Locate the cells, classifying each as a parasitized RBC, an uninfected RBC, or a WBC.
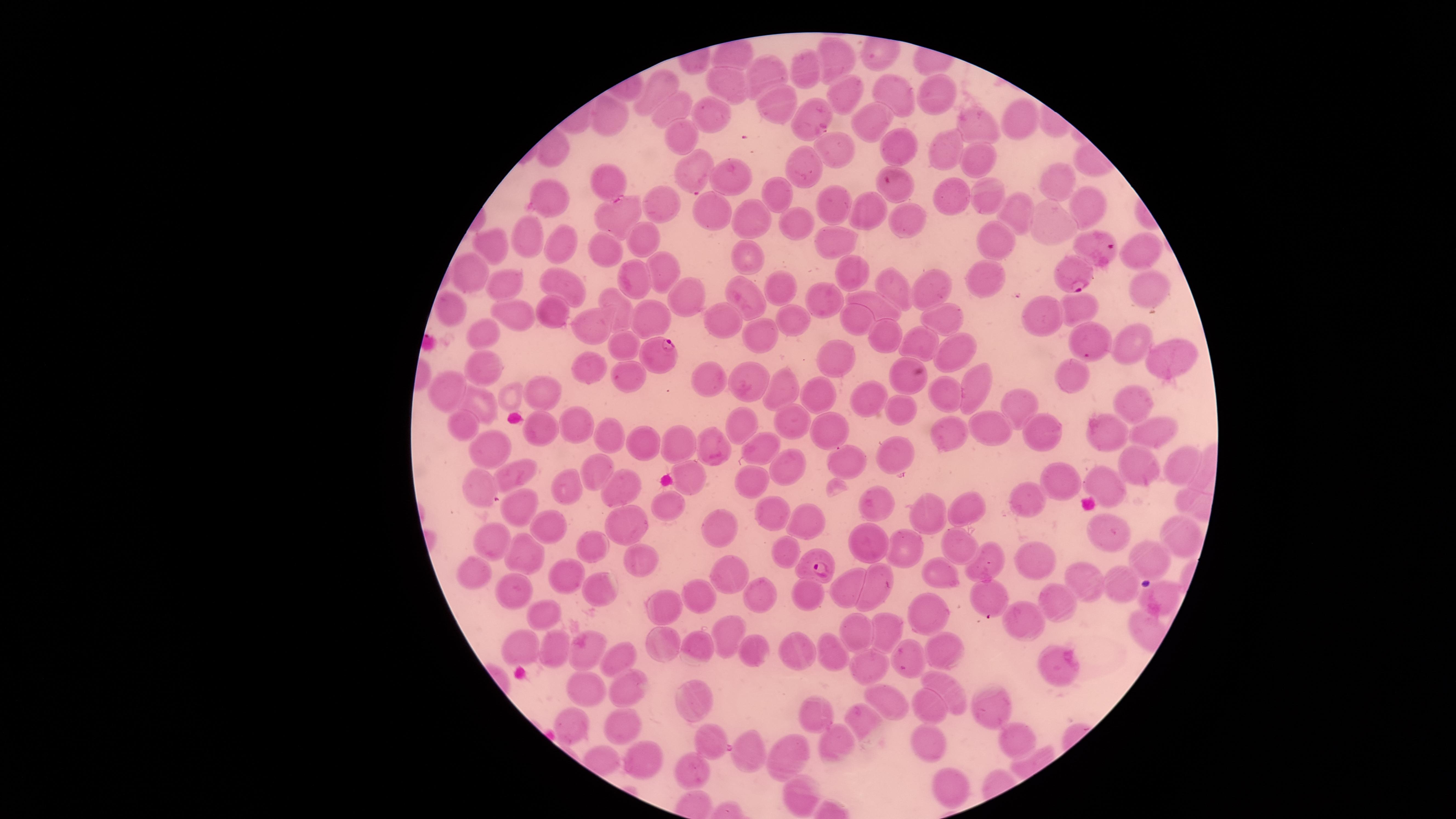
Approximate marker points as [x, y] in pixels.
Parasitized RBCs: [690, 171], [605, 178], [894, 181], [1101, 241], [1072, 273], [661, 352], [810, 564].
Uninfected RBCs: [836, 56], [766, 68], [802, 70], [728, 78], [662, 84], [843, 94], [936, 94], [891, 96], [775, 101], [671, 105], [816, 110], [719, 113], [876, 115], [611, 118], [1017, 118], [975, 125], [684, 135], [896, 144], [948, 149], [835, 150], [972, 162], [806, 167], [733, 178], [1052, 184], [768, 189], [955, 194], [989, 195], [543, 197], [1089, 199], [835, 202], [659, 205], [716, 211], [1011, 211], [866, 213], [619, 217], [752, 218], [906, 218], [1053, 224], [800, 226], [529, 239], [649, 239], [835, 239], [1001, 243], [497, 244], [558, 244], [1136, 250], [612, 252], [751, 253], [850, 269], [663, 271], [474, 274], [983, 277], [638, 279], [564, 282], [777, 284], [892, 287], [506, 288], [934, 288], [687, 289], [1149, 293], [751, 295], [818, 298], [1076, 305], [877, 307], [452, 309], [552, 310], [622, 310], [519, 315], [788, 316], [661, 317], [946, 317], [1043, 317], [855, 320], [714, 323], [602, 324], [483, 329], [880, 334], [1088, 339], [622, 344], [763, 344], [917, 346], [1126, 346], [957, 348], [830, 356], [1167, 357], [486, 366], [596, 370], [628, 372], [1077, 375], [717, 378], [901, 380], [752, 383], [784, 383], [450, 386], [545, 390], [975, 390], [945, 395], [825, 398], [871, 399], [1132, 399], [477, 402], [1020, 407], [896, 410], [793, 420], [578, 422], [747, 422], [465, 426], [545, 428], [991, 429], [946, 431], [832, 432], [1041, 433], [1102, 434], [1153, 434], [610, 437], [712, 442], [754, 445], [492, 446], [645, 447], [677, 447], [896, 452], [848, 455], [794, 463], [1136, 467], [1182, 467], [598, 469], [692, 470], [514, 474], [749, 476], [1109, 476], [1059, 478], [481, 486], [568, 487], [626, 487], [1021, 500], [671, 503], [968, 506], [875, 508], [521, 510], [775, 510], [924, 511], [722, 521], [807, 521], [626, 524], [547, 529], [1105, 529], [1181, 534], [874, 540], [592, 542], [494, 543], [957, 547], [520, 550], [784, 550], [901, 550], [991, 556], [1146, 557], [1035, 560], [650, 562], [942, 570], [572, 571], [478, 574], [733, 575], [876, 582], [1084, 582], [1120, 583], [845, 584], [598, 586], [516, 592], [807, 592], [700, 593], [992, 595], [765, 598], [1057, 598], [1155, 600], [669, 604], [545, 610], [922, 612], [1029, 620], [729, 630], [858, 632], [893, 635], [524, 642], [663, 644], [695, 644], [551, 647], [907, 648], [828, 650], [943, 651], [757, 652], [795, 652], [584, 655], [616, 655], [1061, 662], [867, 666], [585, 686], [623, 686], [952, 687], [690, 697], [891, 700], [995, 705], [928, 706], [814, 714], [867, 722], [573, 723], [621, 723], [1012, 739], [922, 740], [712, 741], [840, 743], [751, 756], [643, 759], [775, 759], [690, 774], [943, 776], [797, 791].
No WBCs identified.

species: Plasmodium falciparum
preparation: thin blood smear
visible_region: circular
stain: Giemsa
image_size: 1456×819 pixels
capture: smartphone photograph through the microscope eyepiece
field_of_view: single